Outline platelets.
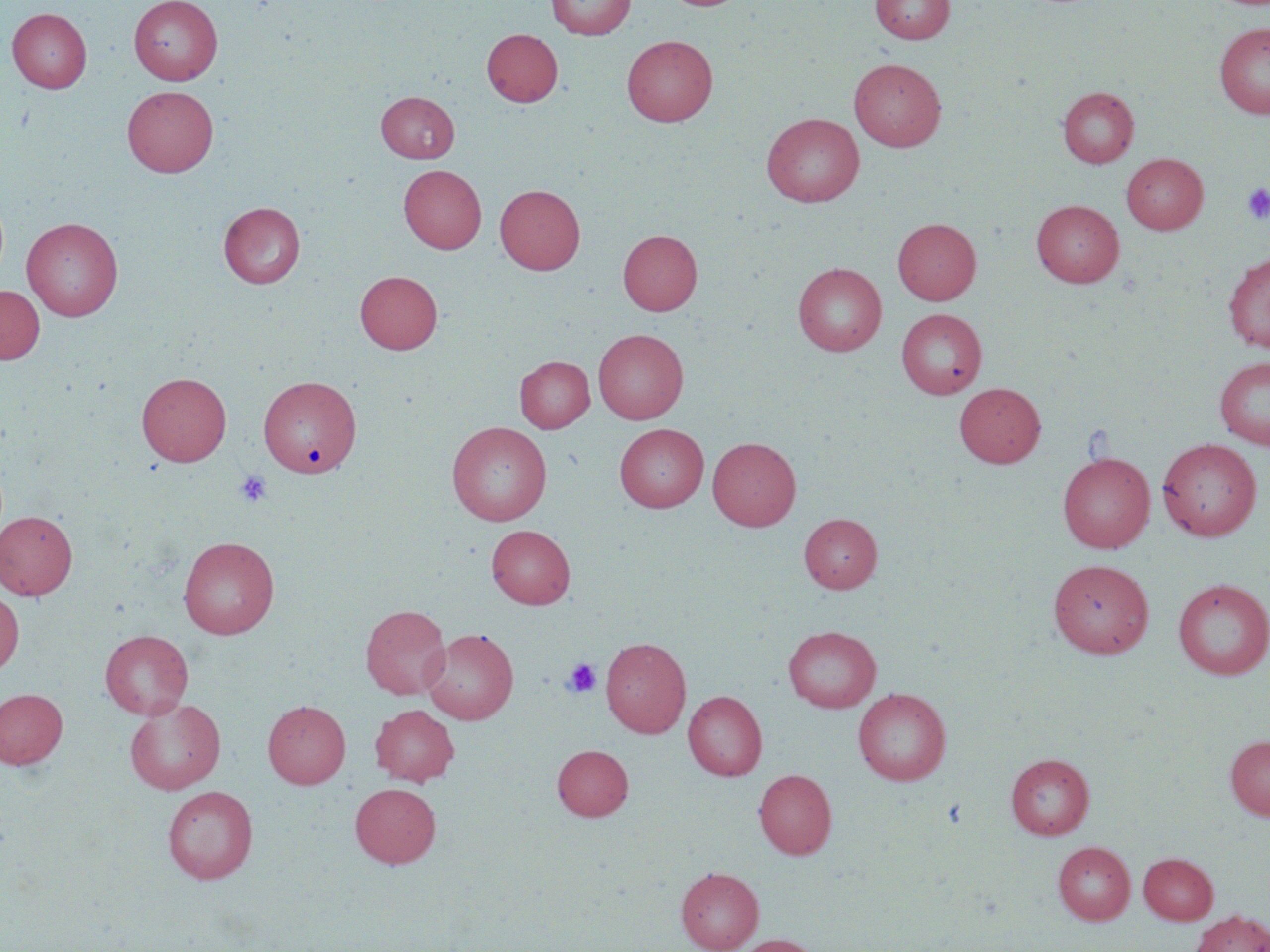
Approximate bounding boxes as [x1, y1, x2, y2] in pixels.
Platelets: [1242, 183, 1270, 223], [234, 470, 273, 508], [562, 658, 601, 698].

Uninfected red blood cell locations: [129, 0, 222, 85], [546, 0, 635, 39], [870, 0, 955, 44], [7, 8, 92, 93], [1214, 22, 1270, 119], [482, 28, 563, 107], [622, 35, 717, 127], [849, 58, 946, 151], [122, 85, 219, 177], [1058, 87, 1139, 167], [376, 91, 459, 163], [762, 113, 865, 207], [1121, 153, 1208, 234], [398, 164, 486, 254], [495, 185, 585, 275], [1031, 199, 1124, 287], [218, 202, 305, 288], [22, 217, 123, 321], [893, 218, 981, 304], [618, 229, 703, 315], [1223, 252, 1270, 352], [793, 262, 887, 356], [355, 270, 443, 354], [0, 285, 45, 364], [896, 308, 987, 399], [593, 328, 688, 424], [515, 356, 595, 432], [1214, 356, 1270, 449], [137, 372, 232, 466], [259, 375, 361, 477], [955, 382, 1045, 467], [447, 421, 552, 526], [615, 423, 709, 512], [708, 437, 801, 530], [1157, 438, 1262, 541], [1057, 451, 1155, 553], [0, 510, 78, 599], [799, 513, 882, 592], [486, 525, 575, 609], [178, 536, 280, 639], [1048, 559, 1154, 658], [1172, 578, 1270, 680], [0, 589, 24, 676], [360, 605, 451, 699], [783, 625, 881, 713], [422, 628, 519, 724], [100, 630, 193, 719], [600, 636, 691, 738], [0, 688, 68, 768], [853, 688, 951, 786], [683, 691, 767, 781], [125, 698, 226, 795], [263, 700, 351, 788], [370, 704, 459, 786], [1224, 735, 1270, 820], [552, 744, 633, 820], [1006, 753, 1094, 839], [754, 769, 837, 860], [350, 782, 441, 868], [162, 786, 258, 884], [1053, 841, 1135, 924], [1139, 852, 1218, 924], [676, 866, 763, 951], [1190, 910, 1270, 952], [731, 934, 822, 952]. Slide-level diagnosis: negative for blood parasites. Thin blood smear. Captured at 1000x magnification. May-Grünwald-Giemsa stain. Image is 1270×952 pixels. Optical microscopy. One field of a larger specimen.